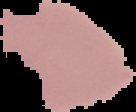
Malaria status: uninfected. Segmented cell region on a black background. From a thin blood film. Image is 136×112 pixels.